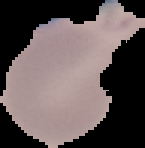 Cell region segmented out of the field of view; the surrounding area is masked to black. Image is 145×148 pixels. Result: no malaria parasites detected. From a thin blood film.